Point out leukocytes.
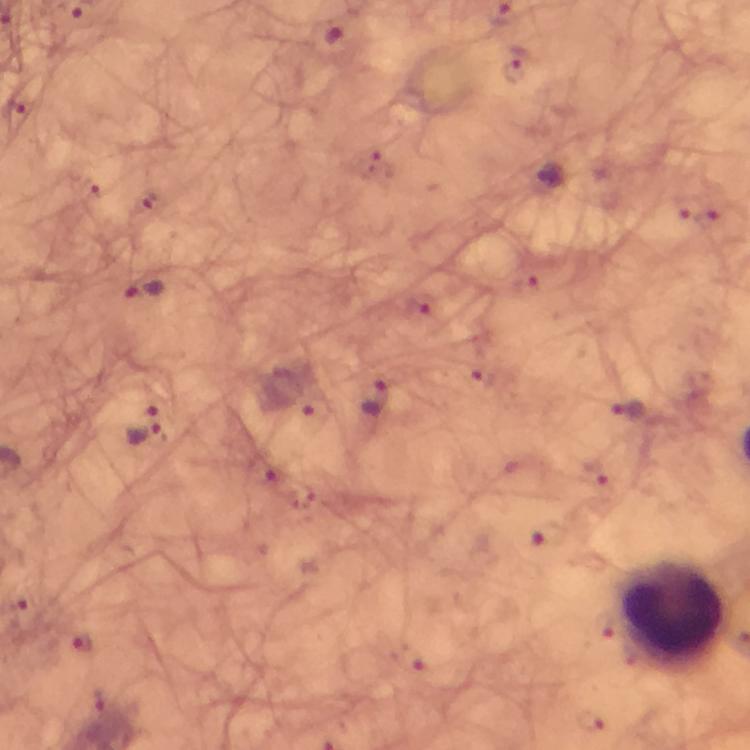
Approximate centers as (x, y) in pixels.
Leukocytes: (673, 610).

capture = smartphone camera through the microscope
cropped from = one field of view
preparation = thick blood film
image size = 750×750 pixels
context = from a diagnostic examination for malaria
stain = Giemsa
immersion oil = used
Plasmodium parasite locations = approximate centers as (x, y) in pixels: (330, 34), (516, 72), (150, 205), (143, 290), (376, 398), (629, 412), (146, 427), (85, 643)
magnification = 100x